Describe the morphology of the erythrocytes.
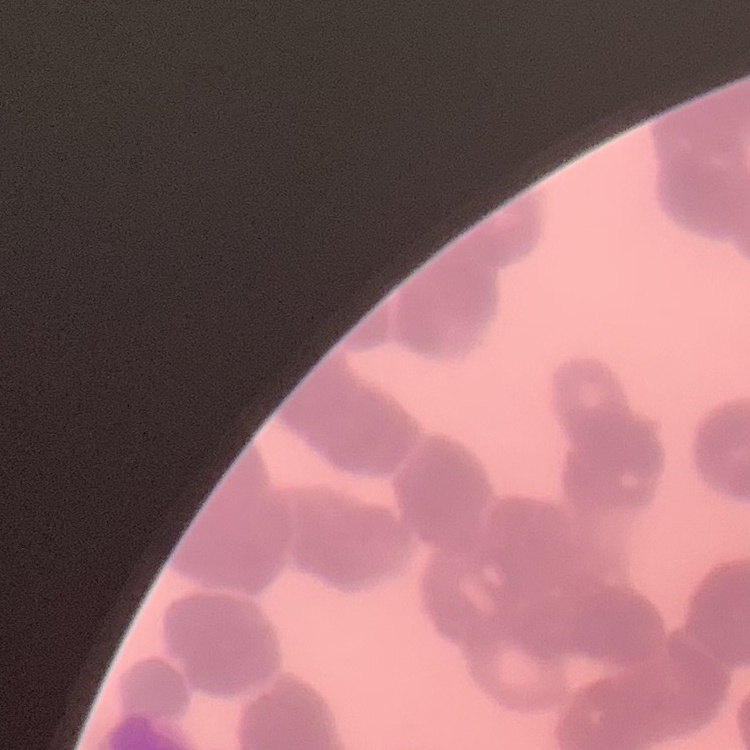
They show rouleaux formation.

Summary:
  - Image type: one tile cut from a larger photomicrograph
  - Preparation: thin blood film
  - Stain: Field's or Giemsa